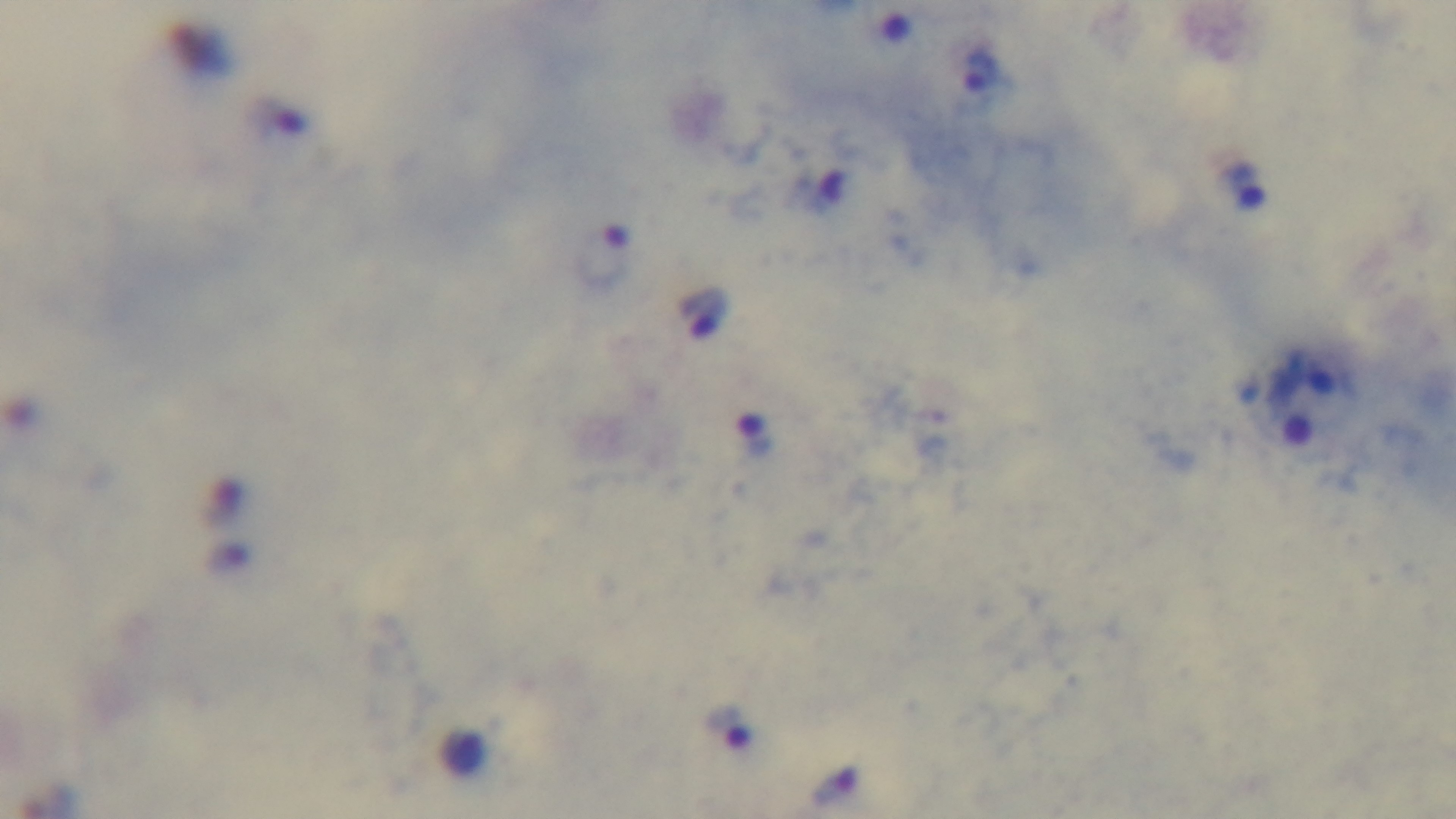
Single field of view. Giemsa-stained. Light microscopy. Preparation: thick smear. Captured with a mounted 4K digital camera. Oil-immersion objective, 100x. Malaria status: infected.